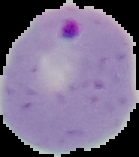

Summary:
  - Image type: segmented cell region with the area outside set to black
  - Malaria status: parasitized
  - Image size: 139×157 pixels
  - Preparation: thin blood film